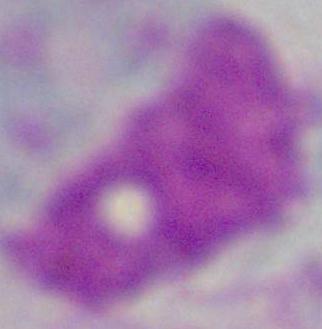
{
  "identification": "leukocyte",
  "modality": "micrograph",
  "magnification": "1000x"
}